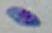

{
  "magnification": "1000x",
  "modality": "micrograph",
  "identification": "Toxoplasma gondii"
}